Assess this cell for malaria.
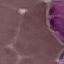

It is uninfected.

Summary:
  - Capture: smartphone camera at the microscope eyepiece
  - Preparation: thin blood film
  - Image type: cell patch, automatically extracted from a larger field of view and resized to 64 × 64 pixels
  - Stain: Giemsa